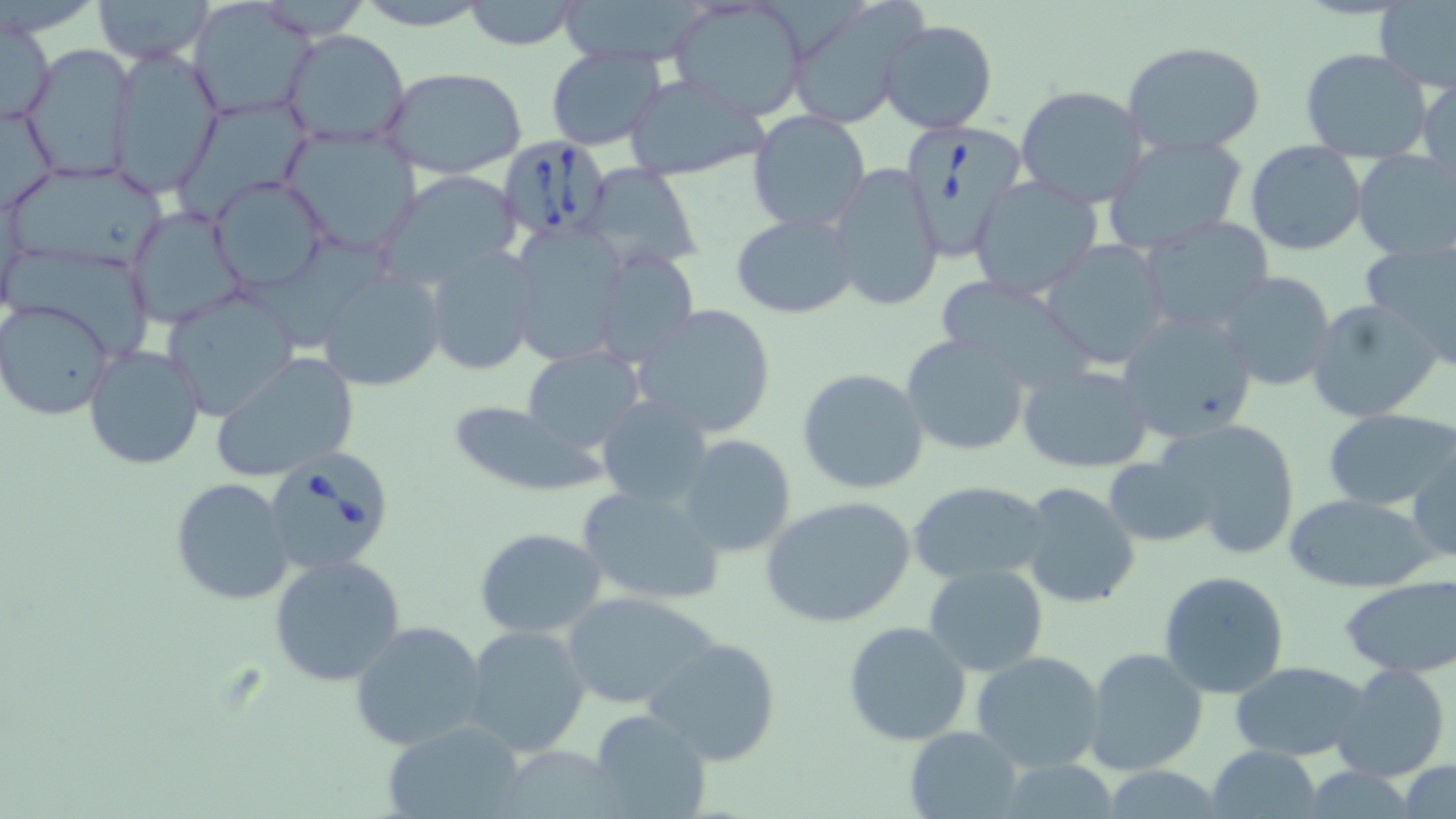
Approximate bounding boxes as named x1/y1/x2/y2 corners in pixels. Babesia divergens-infected red blood cell locations: (x1=900, y1=122, x2=1029, y2=262), (x1=498, y1=136, x2=614, y2=240), (x1=261, y1=446, x2=396, y2=576). Uninfected red blood cell locations: (x1=90, y1=0, x2=216, y2=66), (x1=352, y1=0, x2=494, y2=29), (x1=461, y1=0, x2=584, y2=50), (x1=668, y1=0, x2=812, y2=122), (x1=783, y1=1, x2=927, y2=128), (x1=1375, y1=1, x2=1456, y2=91), (x1=190, y1=2, x2=315, y2=118), (x1=678, y1=4, x2=799, y2=119), (x1=1, y1=16, x2=55, y2=128), (x1=878, y1=17, x2=997, y2=134), (x1=281, y1=29, x2=411, y2=150), (x1=1121, y1=40, x2=1266, y2=156), (x1=20, y1=43, x2=137, y2=182), (x1=544, y1=45, x2=667, y2=150), (x1=108, y1=46, x2=222, y2=195), (x1=1300, y1=47, x2=1434, y2=161), (x1=381, y1=66, x2=528, y2=178), (x1=1417, y1=73, x2=1455, y2=169), (x1=624, y1=75, x2=769, y2=183), (x1=1016, y1=85, x2=1150, y2=207), (x1=176, y1=98, x2=312, y2=216), (x1=1, y1=102, x2=57, y2=214), (x1=748, y1=109, x2=871, y2=232), (x1=279, y1=125, x2=422, y2=258), (x1=1101, y1=132, x2=1250, y2=255), (x1=1245, y1=142, x2=1368, y2=256), (x1=1350, y1=151, x2=1454, y2=263), (x1=3, y1=161, x2=170, y2=272), (x1=581, y1=163, x2=703, y2=269), (x1=827, y1=163, x2=942, y2=312), (x1=377, y1=170, x2=526, y2=291), (x1=208, y1=176, x2=329, y2=292), (x1=968, y1=176, x2=1105, y2=299), (x1=126, y1=205, x2=245, y2=327), (x1=731, y1=213, x2=858, y2=318), (x1=1139, y1=216, x2=1277, y2=336), (x1=507, y1=221, x2=631, y2=366), (x1=1360, y1=236, x2=1456, y2=366), (x1=1042, y1=238, x2=1172, y2=369), (x1=14, y1=244, x2=158, y2=361), (x1=423, y1=245, x2=540, y2=376), (x1=589, y1=246, x2=699, y2=368), (x1=316, y1=267, x2=445, y2=392), (x1=1215, y1=270, x2=1339, y2=393), (x1=932, y1=275, x2=1097, y2=393), (x1=159, y1=289, x2=300, y2=422), (x1=1305, y1=298, x2=1444, y2=423), (x1=1, y1=299, x2=116, y2=421), (x1=632, y1=304, x2=778, y2=441), (x1=1117, y1=310, x2=1259, y2=447), (x1=900, y1=333, x2=1033, y2=456), (x1=81, y1=342, x2=207, y2=470), (x1=521, y1=347, x2=647, y2=454), (x1=211, y1=352, x2=360, y2=482), (x1=1017, y1=363, x2=1153, y2=473), (x1=796, y1=368, x2=930, y2=495), (x1=597, y1=397, x2=715, y2=508), (x1=445, y1=401, x2=604, y2=496), (x1=1325, y1=409, x2=1456, y2=509), (x1=1161, y1=419, x2=1301, y2=558), (x1=676, y1=435, x2=797, y2=557), (x1=1408, y1=441, x2=1454, y2=564), (x1=1102, y1=448, x2=1217, y2=554), (x1=171, y1=477, x2=294, y2=605), (x1=907, y1=479, x2=1052, y2=586), (x1=1017, y1=481, x2=1142, y2=610), (x1=575, y1=482, x2=728, y2=606), (x1=1283, y1=493, x2=1439, y2=593), (x1=760, y1=495, x2=917, y2=629), (x1=474, y1=528, x2=609, y2=639), (x1=268, y1=555, x2=407, y2=686), (x1=923, y1=565, x2=1049, y2=677), (x1=1159, y1=570, x2=1291, y2=700), (x1=1339, y1=577, x2=1456, y2=676), (x1=562, y1=592, x2=720, y2=710), (x1=350, y1=619, x2=488, y2=750), (x1=842, y1=621, x2=972, y2=746), (x1=464, y1=625, x2=594, y2=758), (x1=643, y1=635, x2=782, y2=768), (x1=1083, y1=648, x2=1208, y2=776), (x1=973, y1=650, x2=1107, y2=774), (x1=1230, y1=659, x2=1371, y2=761), (x1=1333, y1=662, x2=1451, y2=783), (x1=588, y1=710, x2=712, y2=819), (x1=385, y1=722, x2=523, y2=816), (x1=904, y1=726, x2=1024, y2=818), (x1=1209, y1=744, x2=1323, y2=817), (x1=996, y1=760, x2=1124, y2=817), (x1=1399, y1=760, x2=1455, y2=818), (x1=1097, y1=767, x2=1228, y2=818). Slide-level diagnosis: Babesia divergens. Image is 1456×819 pixels. 1000x magnification. Thin blood film. May-Grünwald-Giemsa stain. Single field of view. Light microscopy.